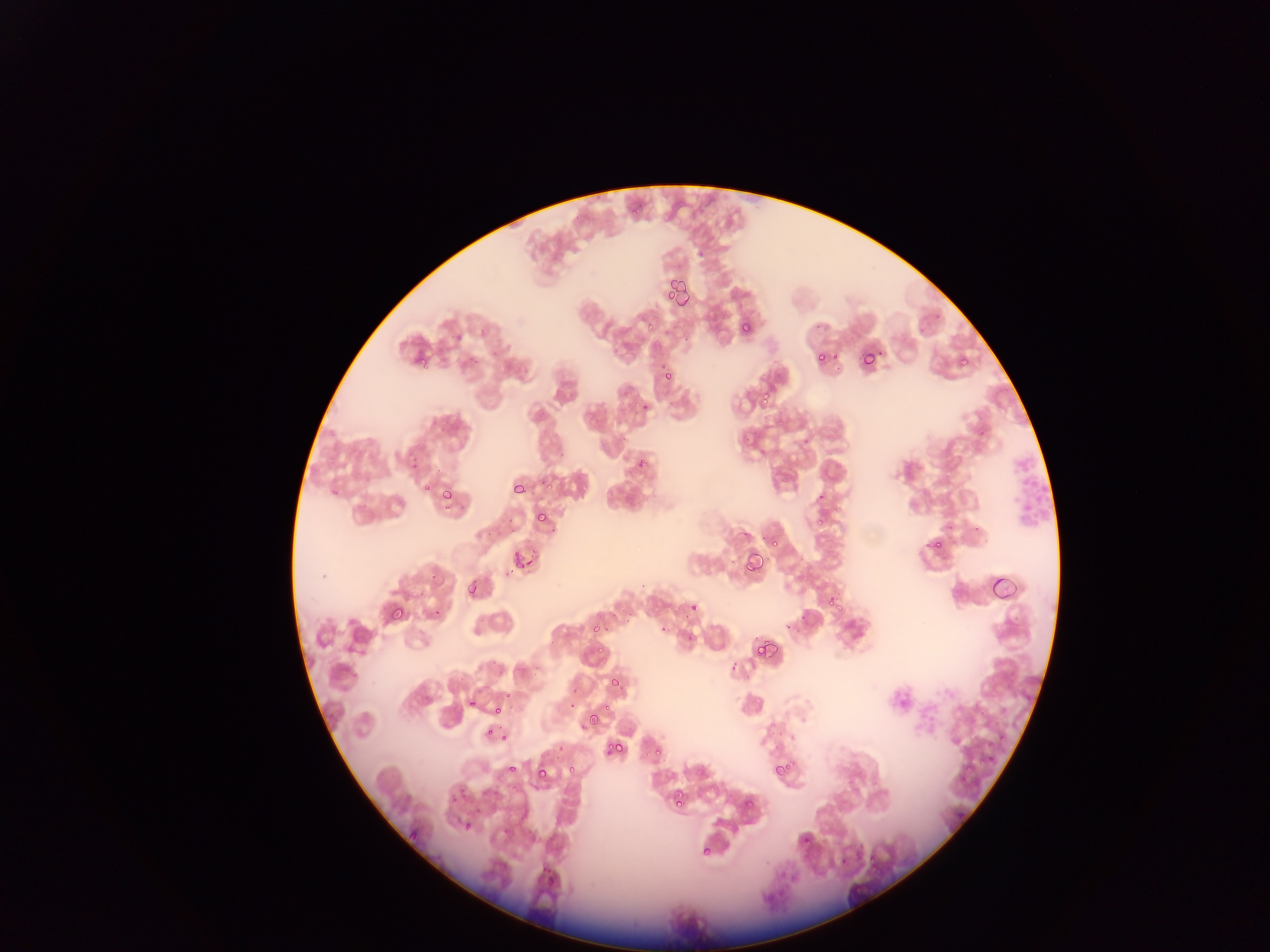

Approximate bounding boxes as (left, top, right, bottom) in pixels. Plasmodium parasite locations: (665, 278, 694, 314), (737, 319, 753, 337), (643, 320, 659, 335), (812, 350, 829, 368), (859, 350, 878, 370), (411, 351, 430, 371), (957, 355, 970, 368), (662, 369, 677, 382), (757, 387, 775, 407), (618, 389, 628, 398), (641, 397, 654, 410), (634, 452, 644, 468), (782, 473, 791, 486), (510, 481, 530, 501), (422, 484, 428, 499), (438, 488, 451, 499), (535, 509, 549, 525), (814, 510, 829, 523), (929, 531, 948, 552), (764, 533, 781, 551), (510, 549, 526, 570), (743, 549, 768, 578), (988, 574, 1014, 602), (467, 582, 480, 598), (827, 590, 839, 607), (688, 601, 699, 610), (393, 606, 409, 622), (590, 619, 604, 635), (754, 639, 776, 661), (594, 642, 604, 653), (609, 675, 624, 691), (570, 694, 579, 714), (468, 695, 476, 708), (492, 698, 505, 715), (602, 700, 613, 712), (588, 711, 602, 734), (484, 727, 494, 739), (500, 735, 509, 747), (608, 742, 626, 753), (653, 749, 662, 759), (771, 760, 792, 782), (505, 762, 515, 773), (560, 765, 580, 778), (538, 772, 550, 785), (508, 788, 519, 797), (742, 793, 757, 808), (671, 794, 684, 811), (462, 822, 473, 833), (695, 842, 710, 857), (866, 850, 882, 869). Single field of view. Thin blood smear. Image is 1270×952 pixels. Collected in Ghana. Mobile-phone photograph taken through the microscope.